State the blood parasite species.
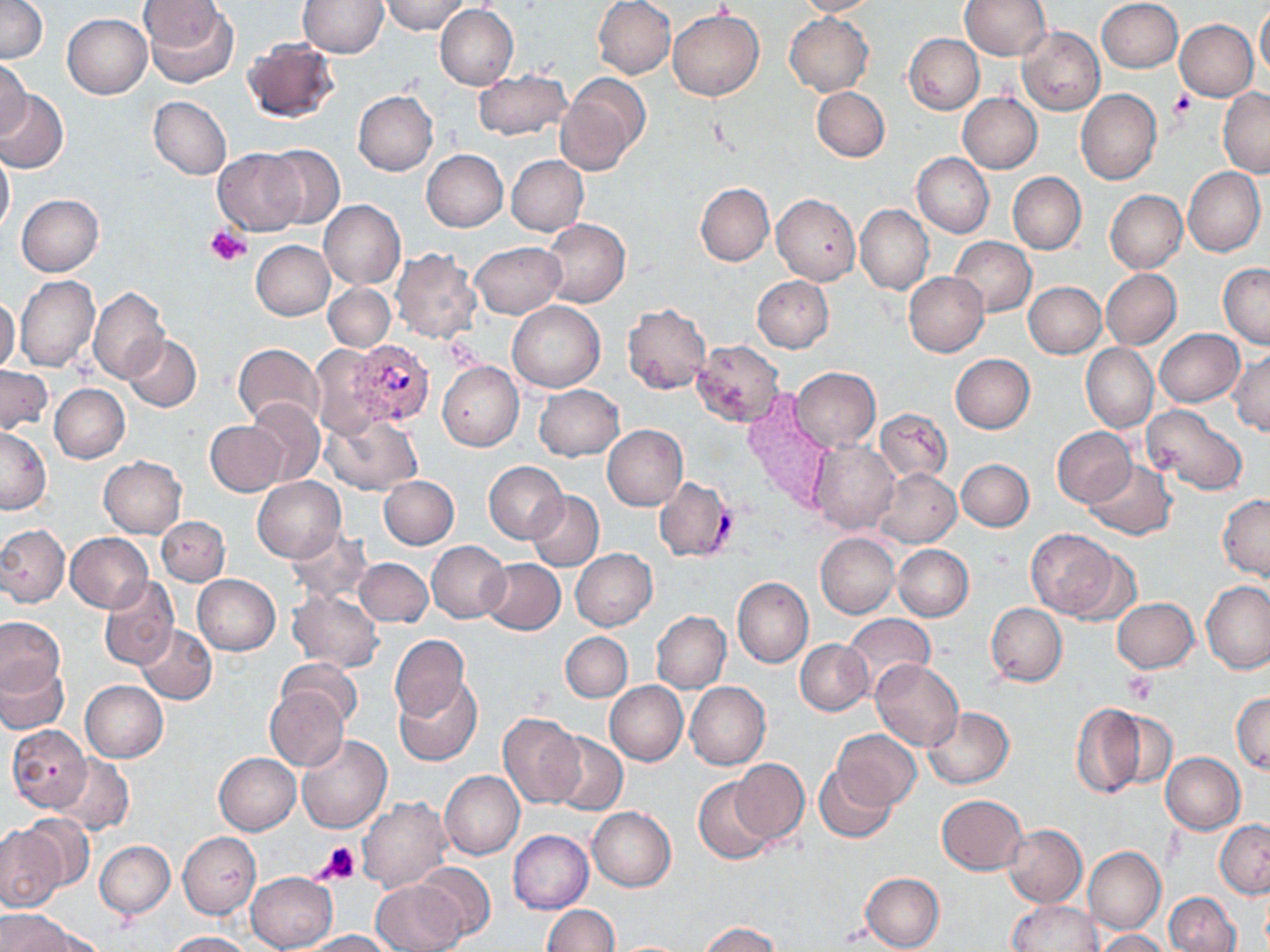

Plasmodium vivax.

Approximate bounding boxes as (x1,y1)-(x2,y2) corner pairs in pixels. Plasmodium vivax-infected red blood cell locations: (343,341)-(438,428), (654,476)-(737,563). Platelet locations: (1168,91)-(1193,121), (205,227)-(250,265), (1121,670)-(1159,703), (317,843)-(361,884). Uninfected red blood cell locations: (0,0)-(47,64), (299,0)-(387,57), (381,0)-(470,34), (593,0)-(676,79), (792,0)-(878,17), (960,0)-(1050,60), (1096,0)-(1182,73), (142,2)-(239,88), (434,5)-(519,89), (1256,5)-(1270,82), (669,10)-(764,101), (784,13)-(873,96), (62,14)-(151,99), (1174,19)-(1258,101), (1017,26)-(1104,116), (904,34)-(984,114), (242,35)-(342,124), (0,60)-(32,139), (472,69)-(571,140), (556,75)-(647,177), (812,87)-(890,161), (1218,88)-(1270,177), (0,89)-(68,173), (1076,89)-(1162,185), (353,90)-(438,176), (958,92)-(1042,173), (148,97)-(231,179), (260,145)-(346,230), (0,147)-(15,234), (213,149)-(307,235), (422,149)-(508,231), (913,152)-(993,238), (506,154)-(588,236), (1183,166)-(1265,257), (1007,172)-(1086,254), (695,183)-(774,266), (1105,190)-(1187,273), (772,193)-(860,286), (17,194)-(103,276), (319,200)-(405,289), (855,205)-(933,294), (542,217)-(630,308), (948,236)-(1036,316), (250,240)-(335,320), (471,242)-(565,317), (390,249)-(481,343), (1219,262)-(1270,350), (1101,268)-(1181,349), (904,271)-(988,357), (14,275)-(99,372), (752,276)-(834,352), (1023,281)-(1106,358), (324,284)-(395,351), (88,288)-(169,383), (0,296)-(20,374), (507,301)-(605,393), (622,304)-(711,393), (1155,328)-(1244,407), (123,335)-(201,411), (691,341)-(786,428), (232,343)-(324,428), (1081,343)-(1158,432), (309,344)-(388,439), (1229,348)-(1270,436), (950,354)-(1035,433), (438,361)-(523,451), (0,366)-(52,433), (791,367)-(881,451), (50,384)-(131,463), (534,384)-(624,461), (740,394)-(831,511), (246,398)-(325,486), (1142,403)-(1249,495), (875,407)-(953,483), (323,413)-(422,495), (205,421)-(288,495), (602,424)-(688,511), (0,426)-(52,514), (1052,427)-(1137,507), (808,439)-(900,535), (98,456)-(187,538), (1082,458)-(1176,540), (956,459)-(1034,531), (485,461)-(569,544), (871,467)-(960,547), (379,475)-(458,549), (252,476)-(345,563), (525,490)-(604,571), (1217,494)-(1270,580), (157,517)-(229,585), (0,525)-(69,606), (284,529)-(371,604), (1026,529)-(1122,619), (815,532)-(901,619), (65,533)-(153,611), (426,540)-(510,622), (893,545)-(973,620), (571,549)-(657,631), (354,558)-(433,627), (480,559)-(565,635), (192,575)-(280,655), (98,576)-(179,670), (732,577)-(813,669), (1200,582)-(1270,673), (287,590)-(384,671), (1112,597)-(1198,672), (985,602)-(1067,686), (651,611)-(731,694), (842,614)-(935,695), (0,617)-(65,696), (136,623)-(217,704), (560,631)-(633,702), (389,635)-(469,721), (796,639)-(873,715), (276,658)-(363,726), (871,659)-(963,751), (0,660)-(69,736), (395,679)-(482,766), (80,681)-(167,762), (605,681)-(687,766), (685,681)-(770,770), (264,686)-(347,771), (1231,691)-(1269,775), (1070,703)-(1148,797), (924,707)-(1013,789), (1097,707)-(1177,793), (499,713)-(586,807), (8,724)-(93,812), (833,730)-(920,809), (548,731)-(628,817), (297,734)-(392,834), (214,752)-(301,835), (1161,752)-(1245,834), (53,756)-(134,834), (730,758)-(809,843), (814,763)-(897,844), (440,770)-(524,859), (693,778)-(776,864), (936,795)-(1026,875), (358,798)-(453,893), (587,807)-(676,891), (18,814)-(96,892), (1215,820)-(1270,898), (1002,823)-(1086,907), (0,827)-(64,910), (509,830)-(593,914), (178,832)-(259,918), (95,840)-(175,917), (1083,845)-(1165,935), (414,863)-(497,941), (246,872)-(338,951), (860,872)-(944,952), (372,880)-(469,951), (1164,892)-(1241,952), (1008,900)-(1100,951), (542,904)-(618,952), (2,909)-(74,952), (699,922)-(782,952), (28,927)-(109,952), (1097,929)-(1170,952), (297,930)-(394,951), (166,932)-(252,952). Captured at 1000x magnification. Single field of view. Thin blood smear. Optical microscopy. Image is 1270×952 pixels. May-Grünwald-Giemsa stain.